Classify this cell by malaria status.
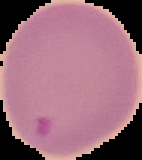

Parasitized.

preparation: thin blood smear
image_type: segmented cell region on a black background
image_size: 142×160 pixels